Locate and identify every blood parasite.
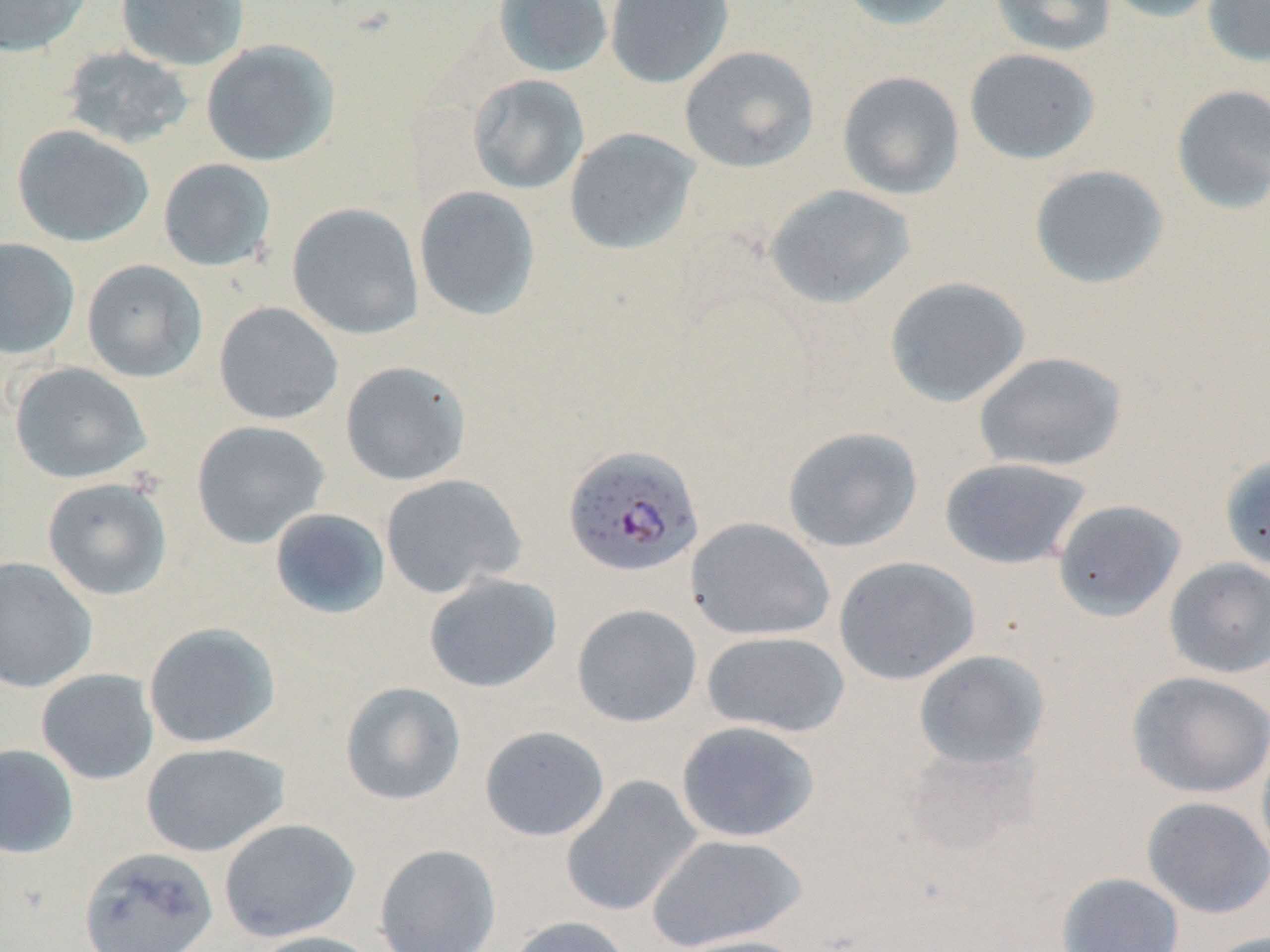

Approximate bounding boxes as named x1/y1/x2/y2 corners in pixels.
Plasmodium falciparum-infected red blood cells: (x1=562, y1=444, x2=705, y2=579).
No Plasmodium ovale, Plasmodium malariae, Plasmodium vivax, Babesia divergens, or Trypanosoma brucei observed.

{
  "slide_level_diagnosis": "Plasmodium falciparum",
  "preparation": "thin blood film",
  "image_size": "1270×952 pixels",
  "uninfected_red_blood_cell_locations": "approximate bounding boxes as named x1/y1/x2/y2 corners in pixels: (x1=0, y1=0, x2=91, y2=57), (x1=115, y1=0, x2=250, y2=71), (x1=493, y1=0, x2=613, y2=78), (x1=605, y1=0, x2=734, y2=89), (x1=834, y1=0, x2=969, y2=31), (x1=989, y1=0, x2=1117, y2=57), (x1=1098, y1=0, x2=1228, y2=23), (x1=1202, y1=0, x2=1270, y2=67), (x1=201, y1=39, x2=340, y2=167), (x1=58, y1=45, x2=196, y2=150), (x1=679, y1=45, x2=819, y2=173), (x1=963, y1=47, x2=1101, y2=165), (x1=836, y1=71, x2=965, y2=201), (x1=467, y1=74, x2=589, y2=195), (x1=1170, y1=84, x2=1270, y2=214), (x1=11, y1=124, x2=155, y2=247), (x1=563, y1=128, x2=701, y2=256), (x1=157, y1=158, x2=277, y2=272), (x1=1029, y1=164, x2=1170, y2=289), (x1=763, y1=184, x2=916, y2=310), (x1=413, y1=185, x2=541, y2=321), (x1=287, y1=202, x2=425, y2=340), (x1=0, y1=237, x2=80, y2=360), (x1=81, y1=259, x2=208, y2=383), (x1=884, y1=276, x2=1031, y2=408), (x1=213, y1=301, x2=344, y2=425), (x1=973, y1=351, x2=1127, y2=473), (x1=340, y1=361, x2=472, y2=486), (x1=9, y1=362, x2=152, y2=484), (x1=191, y1=420, x2=330, y2=549), (x1=782, y1=426, x2=923, y2=553), (x1=1220, y1=453, x2=1270, y2=575), (x1=939, y1=457, x2=1092, y2=570), (x1=379, y1=474, x2=527, y2=598), (x1=41, y1=477, x2=173, y2=601), (x1=1052, y1=499, x2=1187, y2=621), (x1=269, y1=507, x2=391, y2=620), (x1=686, y1=517, x2=836, y2=642), (x1=0, y1=556, x2=97, y2=693), (x1=834, y1=556, x2=981, y2=686), (x1=1163, y1=557, x2=1270, y2=678), (x1=423, y1=573, x2=562, y2=694), (x1=571, y1=603, x2=703, y2=727), (x1=142, y1=622, x2=281, y2=749), (x1=701, y1=631, x2=850, y2=737), (x1=914, y1=649, x2=1050, y2=770), (x1=36, y1=669, x2=159, y2=785), (x1=1127, y1=671, x2=1270, y2=798), (x1=339, y1=681, x2=466, y2=806), (x1=675, y1=721, x2=820, y2=842), (x1=478, y1=725, x2=611, y2=842), (x1=1256, y1=735, x2=1270, y2=868), (x1=140, y1=742, x2=290, y2=857), (x1=0, y1=744, x2=80, y2=859), (x1=559, y1=775, x2=704, y2=917), (x1=1141, y1=795, x2=1270, y2=919), (x1=218, y1=818, x2=360, y2=942), (x1=644, y1=832, x2=808, y2=952), (x1=374, y1=844, x2=502, y2=952), (x1=78, y1=846, x2=219, y2=951), (x1=1057, y1=872, x2=1185, y2=952), (x1=506, y1=915, x2=633, y2=952), (x1=247, y1=930, x2=385, y2=952), (x1=1201, y1=932, x2=1270, y2=952), (x1=667, y1=933, x2=814, y2=952)",
  "field_of_view": "single",
  "modality": "light microscopy",
  "magnification": "1000x",
  "stain": "May-Grünwald-Giemsa"
}